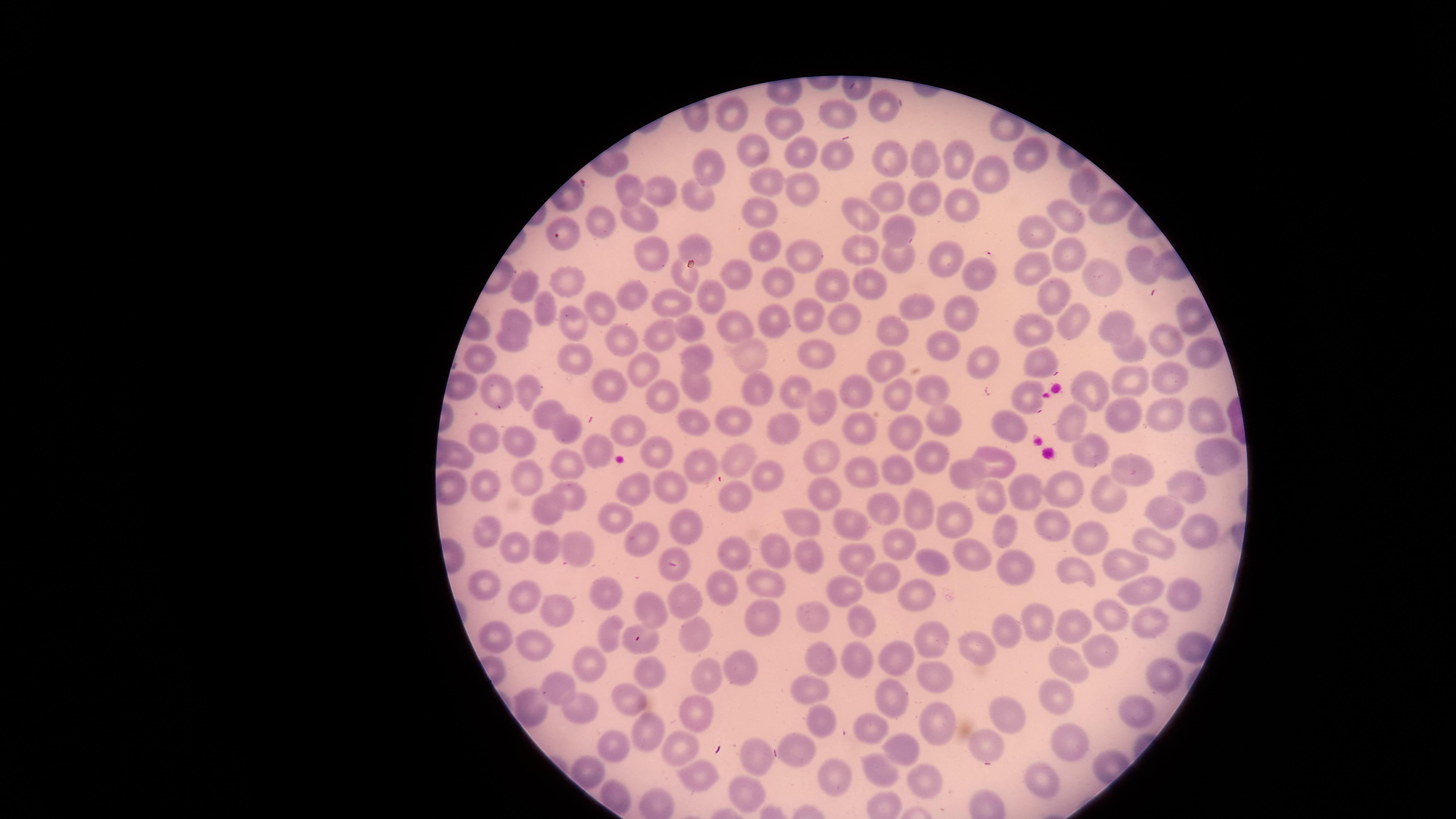 Approximate marker points as {x, y} in pixels. Uninfected RBCs: {883, 104}, {728, 106}, {837, 113}, {789, 119}, {1003, 127}, {793, 146}, {756, 149}, {836, 154}, {1031, 156}, {890, 158}, {956, 158}, {930, 164}, {710, 166}, {988, 178}, {773, 181}, {797, 185}, {1090, 186}, {627, 189}, {658, 194}, {697, 194}, {885, 196}, {928, 205}, {965, 206}, {1111, 208}, {756, 213}, {1062, 215}, {603, 218}, {643, 218}, {863, 218}, {1040, 228}, {896, 231}, {565, 235}, {761, 241}, {694, 246}, {646, 248}, {869, 250}, {1067, 252}, {798, 254}, {901, 255}, {948, 258}, {1144, 263}, {1028, 265}, {974, 269}, {739, 271}, {1102, 275}, {877, 278}, {687, 280}, {521, 283}, {571, 284}, {783, 285}, {832, 287}, {702, 294}, {634, 296}, {1059, 299}, {679, 305}, {923, 307}, {542, 310}, {604, 312}, {841, 314}, {966, 314}, {1190, 316}, {516, 317}, {570, 319}, {805, 320}, {775, 322}, {1031, 324}, {1070, 324}, {1119, 326}, {740, 328}, {687, 330}, {888, 331}, {1163, 334}, {659, 337}, {936, 342}, {616, 344}, {511, 345}, {1130, 347}, {1201, 348}, {698, 353}, {820, 353}, {985, 360}, {480, 363}, {577, 363}, {1041, 363}, {753, 364}, {887, 365}, {641, 369}, {1176, 381}, {1134, 382}, {613, 383}, {527, 386}, {704, 388}, {763, 388}, {856, 389}, {1091, 389}, {938, 390}, {501, 394}, {798, 394}, {900, 394}, {657, 398}, {1027, 400}, {823, 406}, {548, 411}, {1165, 412}, {1123, 415}, {940, 416}, {1203, 416}, {1075, 419}, {731, 421}, {694, 423}, {860, 424}, {568, 427}, {788, 427}, {909, 429}, {632, 431}, {1019, 431}, {490, 440}, {519, 440}, {594, 446}, {656, 450}, {1081, 451}, {1210, 451}, {819, 453}, {458, 455}, {740, 459}, {931, 459}, {571, 461}, {1002, 463}, {702, 465}, {901, 465}, {1127, 470}, {867, 471}, {972, 473}, {761, 474}, {522, 476}, {669, 485}, {1182, 486}, {486, 489}, {637, 489}, {1070, 490}, {1115, 491}, {822, 492}, {1037, 492}, {569, 493}, {735, 494}, {988, 498}, {917, 507}, {890, 509}, {1161, 512}, {545, 514}, {617, 516}, {956, 518}, {809, 523}, {682, 526}, {854, 527}, {483, 528}, {1049, 529}, {1197, 529}, {1009, 534}, {1090, 536}, {638, 542}, {511, 543}, {576, 545}, {1153, 548}, {549, 549}, {894, 550}, {772, 552}, {734, 554}, {811, 555}, {972, 555}, {861, 557}, {937, 561}, {1011, 568}, {1126, 568}, {676, 569}, {1065, 572}, {886, 573}, {768, 585}, {482, 588}, {608, 589}, {720, 590}, {1132, 590}, {850, 591}, {1181, 592}, {921, 598}, {523, 599}, {689, 602}, {648, 605}, {556, 607}, {812, 616}, {1112, 617}, {761, 618}, {858, 618}, {1031, 622}, {1150, 622}, {1068, 625}, {698, 630}, {998, 630}, {611, 632}, {929, 636}, {647, 639}, {498, 640}, {539, 642}, {1188, 643}, {1103, 648}, {970, 649}, {591, 653}, {857, 658}, {893, 658}, {819, 662}, {1068, 665}, {741, 668}, {930, 669}, {652, 670}, {1164, 677}, {711, 680}, {813, 688}, {563, 691}, {626, 695}, {1055, 698}, {893, 699}, {576, 705}, {530, 707}, {1140, 713}, {701, 715}, {818, 723}, {941, 723}, {1014, 725}, {651, 730}, {866, 730}, {1073, 741}, {985, 743}, {897, 747}, {613, 748}, {680, 748}, {802, 752}, {761, 753}, {829, 768}, {881, 769}, {700, 772}, {592, 776}, {923, 779}, {1043, 784}, {747, 791}. Presence: no malaria parasites identified. Image is 1456×819 pixels. Photographed with a smartphone camera through the microscope eyepiece. Circular visible region. Thin blood film. Single field of view. Giemsa stain.